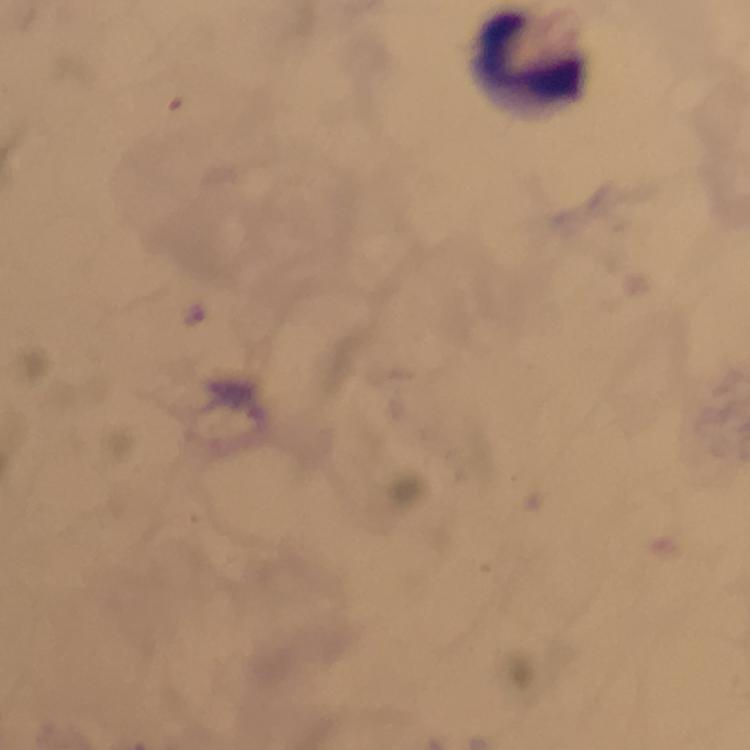

Approximate object centers, in pixels from the top-left corner. Leukocyte locations: (x=533, y=60). Giemsa-stained preparation. Image is 750×750 pixels. At 100x magnification. Malaria parasites: none detected. From a diagnostic examination for malaria. Thick blood smear. Cropped region of a single field of view. Smartphone photograph taken through a microscope. Immersion oil was used.